Name the parasite shown.
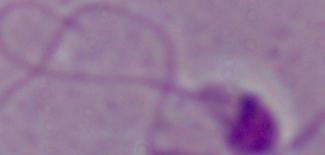
This is Leishmania.

Summary:
  - Magnification: 1000x
  - Modality: photomicrograph